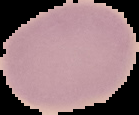

Summary:
  - Image size: 139×115 pixels
  - Image type: segmented cell region with the area outside set to black
  - Preparation: thin blood smear
  - Malaria status: uninfected